Classify this cell by malaria status.
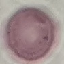
It is uninfected.

Summary:
  - Preparation: thin smear
  - Capture: smartphone camera at the microscope eyepiece
  - Stain: Giemsa
  - Image type: automatically extracted cell patch, resized to 64 × 64 pixels